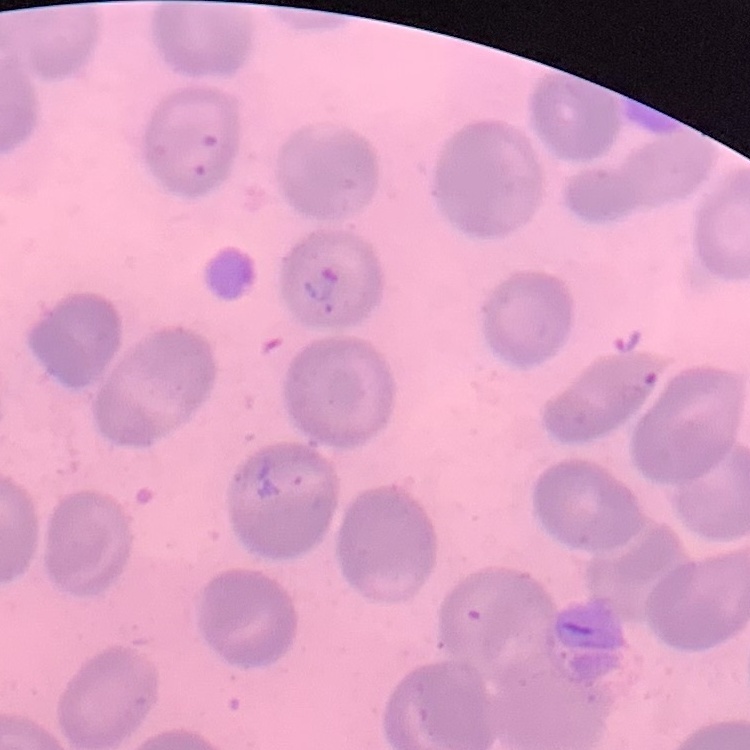

Summary:
  - Erythrocyte morphology: no rouleaux formation
  - Stain: Field's or Giemsa
  - Image type: one tile cut from a larger photomicrograph
  - Preparation: thin blood film